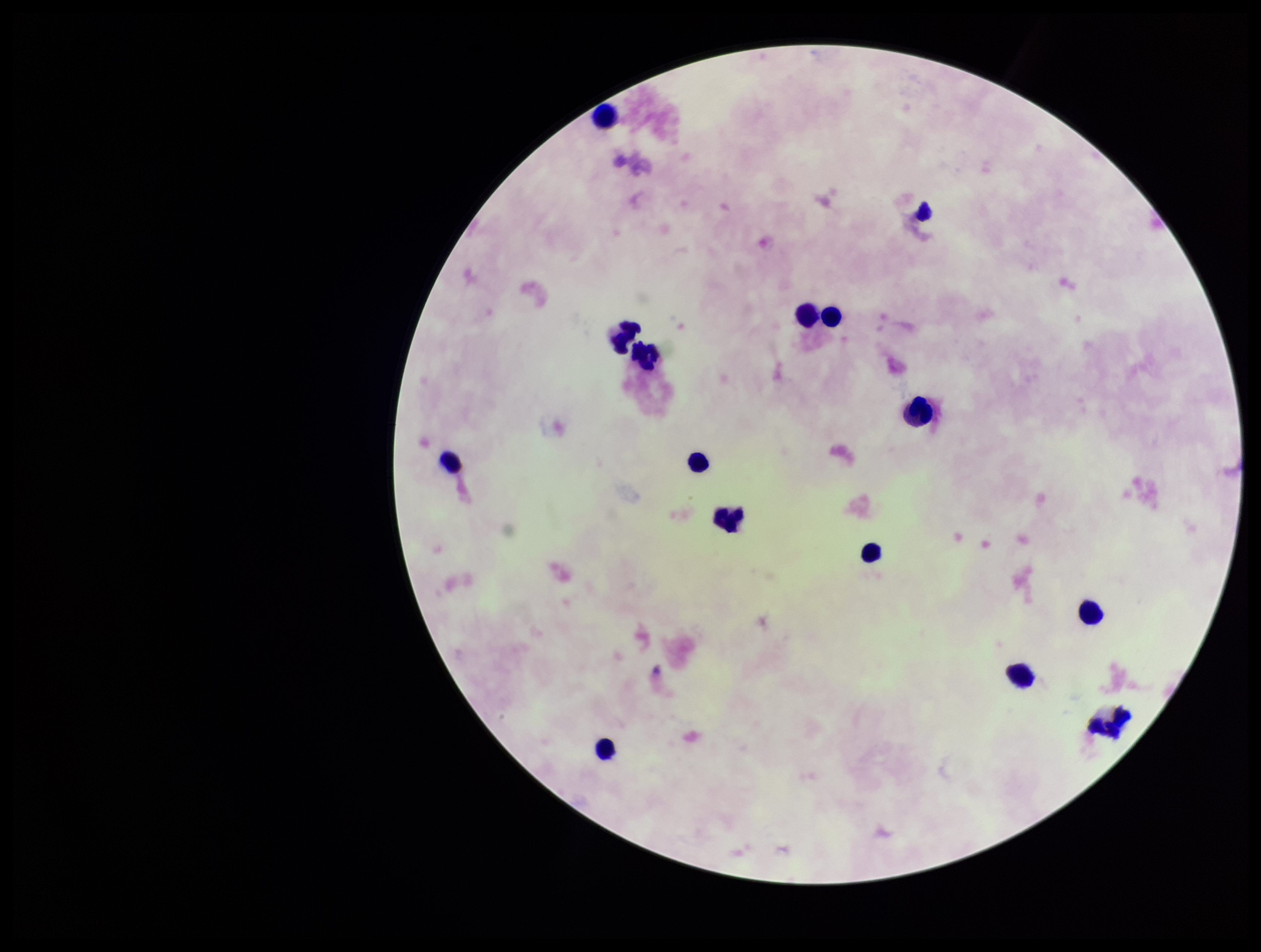 Patient malaria status: negative. One field from this slide. Parasite count: 0. Stained with Giemsa. Smartphone photograph taken through the eyepiece of a microscope. Leukocyte count: 14. Image is 1261×952 pixels. Preparation: thick smear. Plasmodium parasites: none detected.